Classify this cell by malaria status.
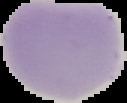

Uninfected.

Summary:
  - Image size: 127×103 pixels
  - Preparation: thin blood film
  - Image type: segmented cell region on a black background